Report the malaria status of this cell.
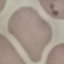
Parasitized.

Summary:
  - Preparation: thin smear
  - Image type: cell patch, automatically extracted from a larger field of view and resized to 64 × 64 pixels
  - Capture: smartphone camera at the microscope eyepiece
  - Stain: Giemsa